Point out each malaria parasite.
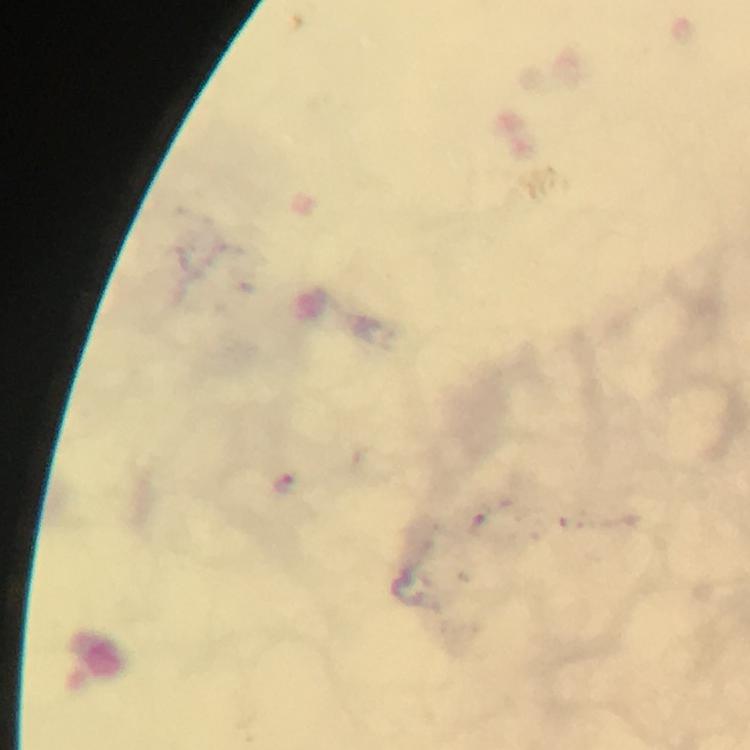

Approximate centers as (x, y) in pixels.
Malaria parasites: (286, 482).

context = from a malaria diagnostic workup
magnification = 100x
immersion oil = applied
stain = Giemsa
cropped from = one field of view
preparation = thick smear
image size = 750×750 pixels
capture = smartphone mounted on the microscope